Give the preparation type.
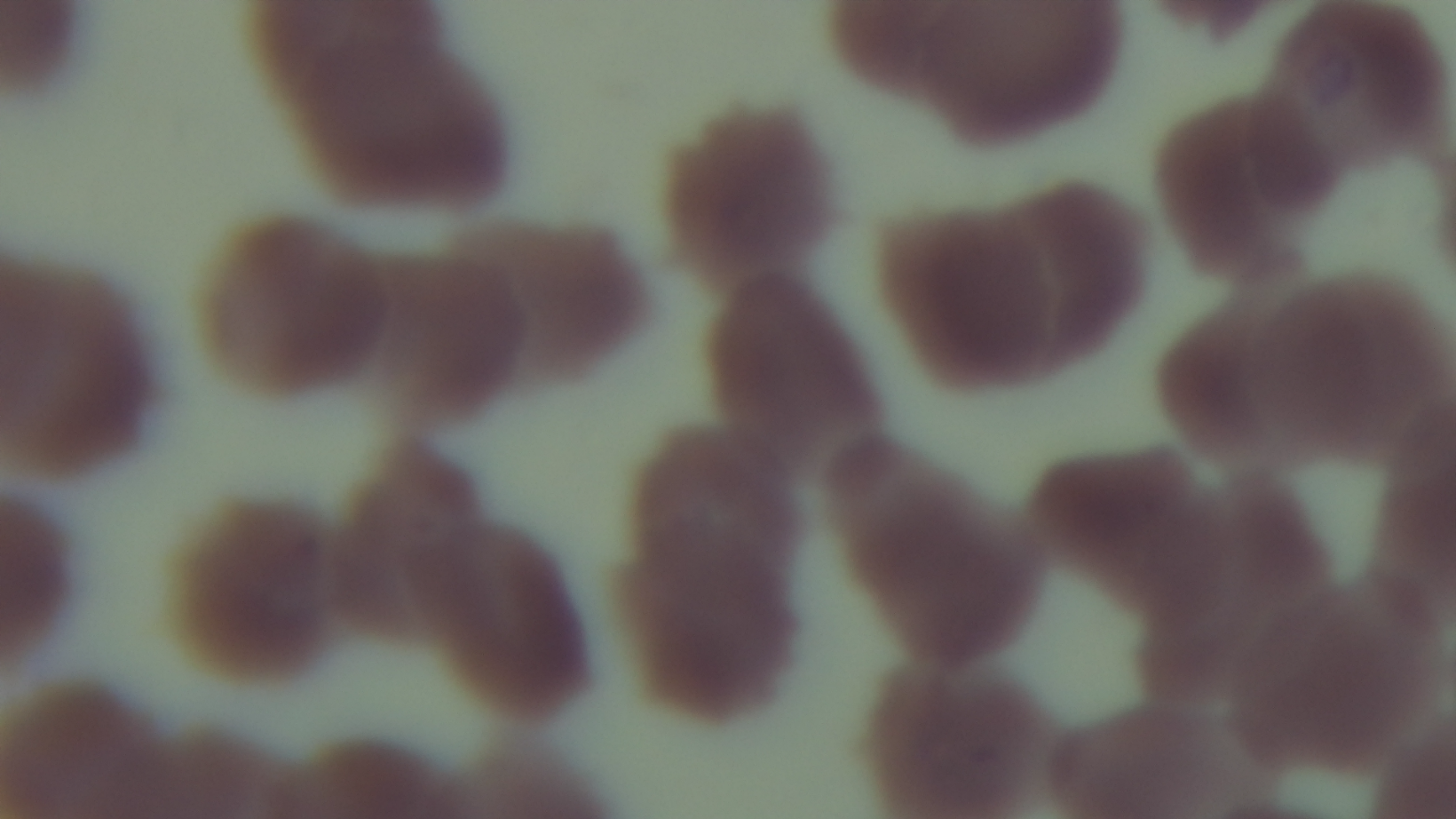

Thin.

Summary:
  - Modality: light microscopy
  - Objective: 100x oil immersion
  - Malaria status: uninfected
  - Stain: Giemsa
  - Field of view: one from the slide
  - Capture: mounted 4K digital camera